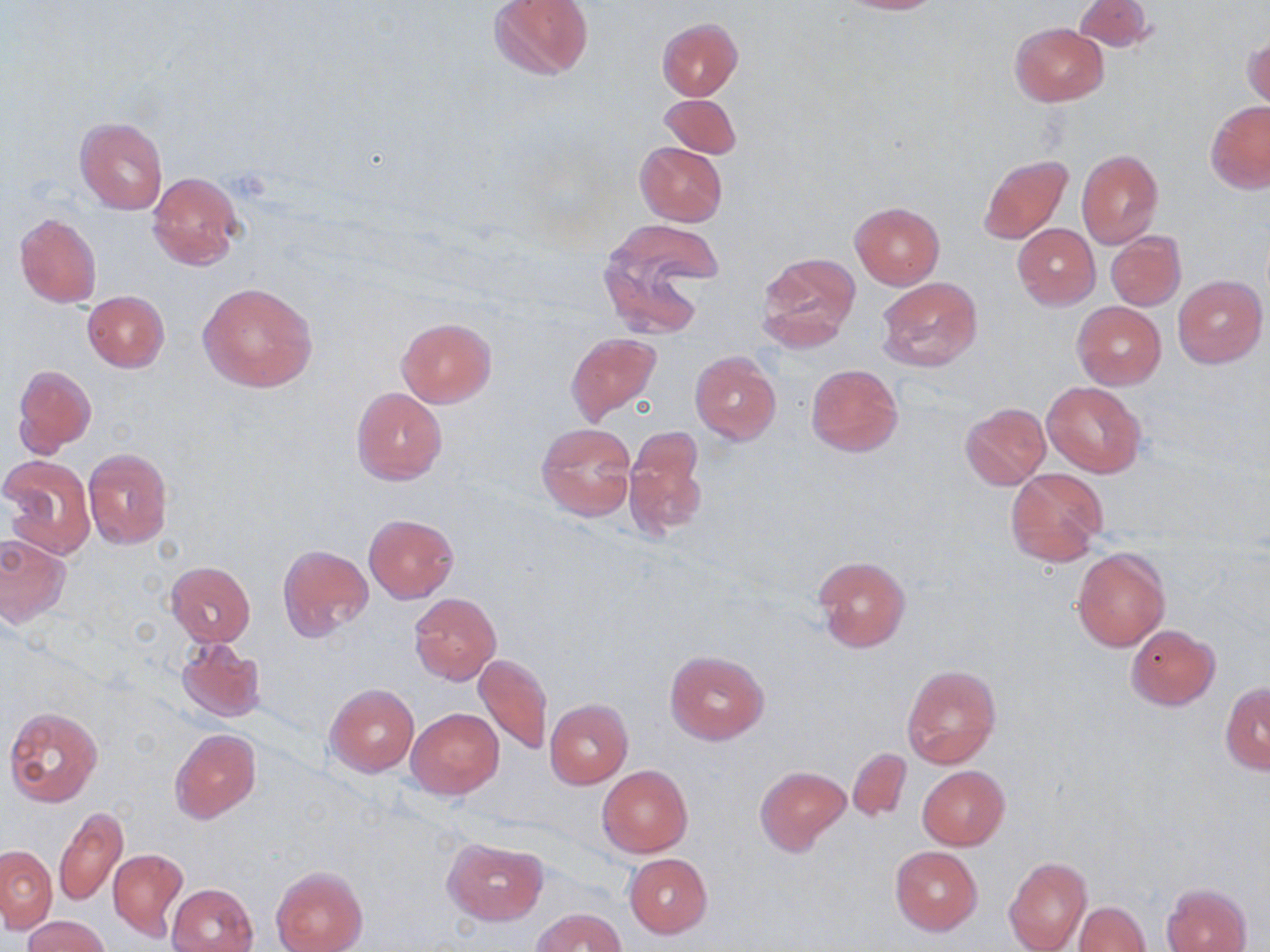
Approximate bounding boxes as named x1/y1/x2/y2 corners in pixels. Platelet locations: (x1=228, y1=167, x2=274, y2=201). Uninfected red blood cell locations: (x1=489, y1=0, x2=593, y2=81), (x1=825, y1=0, x2=947, y2=14), (x1=1073, y1=0, x2=1154, y2=54), (x1=657, y1=18, x2=744, y2=100), (x1=1010, y1=23, x2=1108, y2=105), (x1=1243, y1=33, x2=1269, y2=110), (x1=660, y1=94, x2=740, y2=158), (x1=1206, y1=101, x2=1270, y2=193), (x1=74, y1=116, x2=169, y2=215), (x1=634, y1=142, x2=728, y2=227), (x1=1076, y1=149, x2=1163, y2=248), (x1=978, y1=153, x2=1073, y2=244), (x1=148, y1=172, x2=244, y2=270), (x1=849, y1=202, x2=945, y2=289), (x1=14, y1=212, x2=103, y2=308), (x1=601, y1=221, x2=719, y2=329), (x1=1013, y1=223, x2=1100, y2=310), (x1=1106, y1=232, x2=1185, y2=311), (x1=758, y1=251, x2=860, y2=346), (x1=1172, y1=274, x2=1267, y2=368), (x1=876, y1=276, x2=983, y2=373), (x1=198, y1=281, x2=319, y2=393), (x1=83, y1=291, x2=169, y2=372), (x1=1073, y1=302, x2=1166, y2=389), (x1=396, y1=316, x2=496, y2=407), (x1=566, y1=333, x2=660, y2=422), (x1=690, y1=351, x2=780, y2=445), (x1=804, y1=363, x2=903, y2=457), (x1=13, y1=364, x2=97, y2=455), (x1=1043, y1=381, x2=1146, y2=477), (x1=352, y1=388, x2=447, y2=485), (x1=959, y1=403, x2=1051, y2=491), (x1=536, y1=423, x2=637, y2=522), (x1=623, y1=425, x2=708, y2=540), (x1=82, y1=448, x2=174, y2=550), (x1=2, y1=456, x2=96, y2=558), (x1=1005, y1=467, x2=1108, y2=567), (x1=363, y1=514, x2=457, y2=603), (x1=0, y1=534, x2=70, y2=626), (x1=277, y1=543, x2=373, y2=642), (x1=1072, y1=548, x2=1170, y2=651), (x1=814, y1=555, x2=910, y2=652), (x1=165, y1=561, x2=255, y2=645), (x1=409, y1=592, x2=502, y2=685), (x1=1126, y1=625, x2=1220, y2=710), (x1=176, y1=637, x2=265, y2=724), (x1=664, y1=650, x2=770, y2=744), (x1=475, y1=653, x2=552, y2=755), (x1=902, y1=664, x2=1000, y2=770), (x1=326, y1=683, x2=419, y2=777), (x1=1220, y1=683, x2=1270, y2=773), (x1=544, y1=699, x2=633, y2=788), (x1=3, y1=707, x2=105, y2=808), (x1=406, y1=707, x2=503, y2=799), (x1=170, y1=729, x2=260, y2=824), (x1=847, y1=748, x2=911, y2=823), (x1=597, y1=765, x2=693, y2=858), (x1=756, y1=766, x2=850, y2=855), (x1=918, y1=766, x2=1010, y2=850), (x1=55, y1=807, x2=129, y2=908), (x1=443, y1=837, x2=548, y2=925), (x1=1, y1=845, x2=55, y2=933), (x1=890, y1=846, x2=982, y2=934), (x1=108, y1=848, x2=188, y2=939), (x1=624, y1=854, x2=713, y2=938), (x1=1004, y1=857, x2=1091, y2=951), (x1=272, y1=865, x2=367, y2=952), (x1=166, y1=882, x2=258, y2=952), (x1=1162, y1=883, x2=1252, y2=952), (x1=1074, y1=901, x2=1151, y2=952), (x1=532, y1=907, x2=625, y2=952), (x1=25, y1=915, x2=108, y2=951). Slide-level diagnosis: no evidence of blood parasites. Image is 1270×952 pixels. May-Grünwald-Giemsa stain. Optical microscopy. Thin blood smear. 1000x magnification. Single field of view.